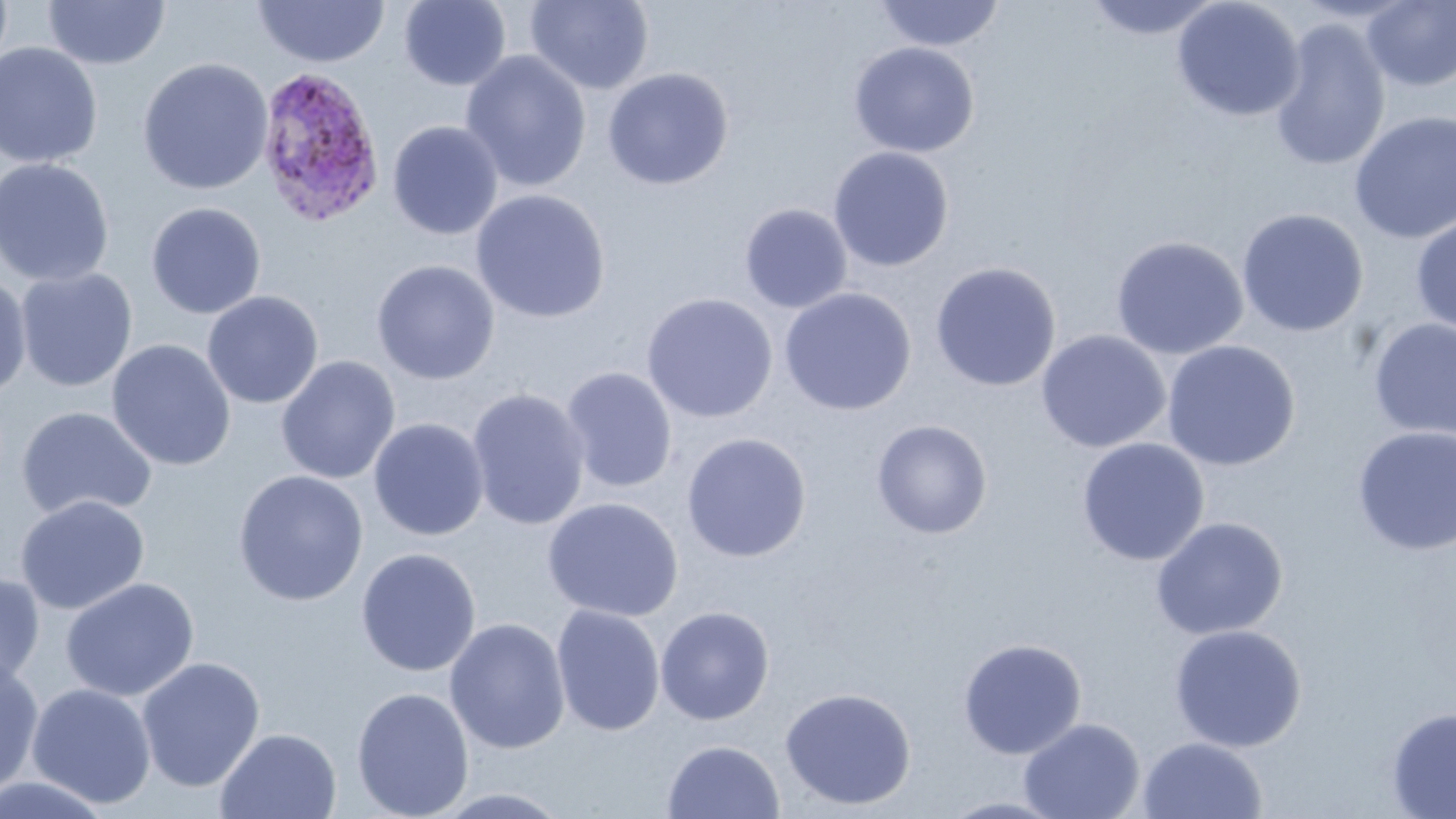
Summary:
  - Coordinate format: approximate bounding boxes as (x1, y1, x2, y2) in pixels
  - Uninfected red blood cell locations: (42, 0, 170, 70), (398, 0, 512, 91), (525, 0, 654, 94), (873, 0, 1005, 52), (1084, 0, 1223, 40), (1171, 0, 1305, 121), (253, 1, 390, 68), (1362, 1, 1456, 91), (1269, 18, 1391, 173), (0, 42, 103, 169), (848, 42, 979, 157), (460, 50, 592, 193), (137, 57, 273, 195), (602, 67, 734, 190), (1349, 110, 1456, 244), (387, 120, 504, 240), (828, 146, 954, 271), (0, 158, 115, 287), (471, 189, 611, 323), (146, 201, 266, 319), (739, 204, 853, 313), (1235, 207, 1369, 337), (1410, 215, 1456, 336), (1110, 235, 1248, 360), (371, 259, 500, 385), (930, 261, 1062, 392), (15, 267, 138, 392), (0, 272, 33, 404), (779, 287, 917, 415), (202, 290, 323, 409), (641, 293, 778, 423), (1368, 318, 1456, 440), (1036, 329, 1171, 453), (107, 339, 235, 471), (1161, 340, 1301, 471), (275, 355, 400, 485), (561, 366, 678, 494), (466, 388, 592, 531), (16, 406, 158, 521), (369, 418, 489, 540), (871, 419, 993, 539), (1352, 425, 1456, 556), (681, 432, 812, 562), (1076, 437, 1210, 566), (233, 469, 369, 606), (15, 495, 150, 615), (543, 497, 684, 622), (1150, 516, 1288, 640), (356, 547, 481, 677), (0, 572, 45, 691), (59, 577, 200, 702), (551, 605, 665, 736), (655, 606, 775, 725), (444, 618, 571, 755), (1168, 623, 1307, 752), (958, 638, 1086, 760), (0, 656, 44, 798), (136, 656, 265, 792), (26, 682, 157, 809), (351, 686, 474, 819), (780, 687, 916, 810), (1385, 707, 1456, 818), (1018, 716, 1145, 819), (215, 727, 342, 818), (1137, 735, 1268, 818), (662, 739, 785, 819), (0, 773, 116, 818), (430, 787, 573, 818), (939, 795, 1070, 818)
  - Plasmodium ovale-infected red blood cell locations: (254, 64, 385, 228)
  - Slide-level diagnosis: Plasmodium ovale
  - Image size: 1456×819 pixels
  - Stain: May-Grünwald-Giemsa
  - Preparation: thin blood smear
  - Modality: optical microscopy
  - Magnification: 1000x
  - Field of view: one of a larger specimen